Describe the morphology of the erythrocytes.
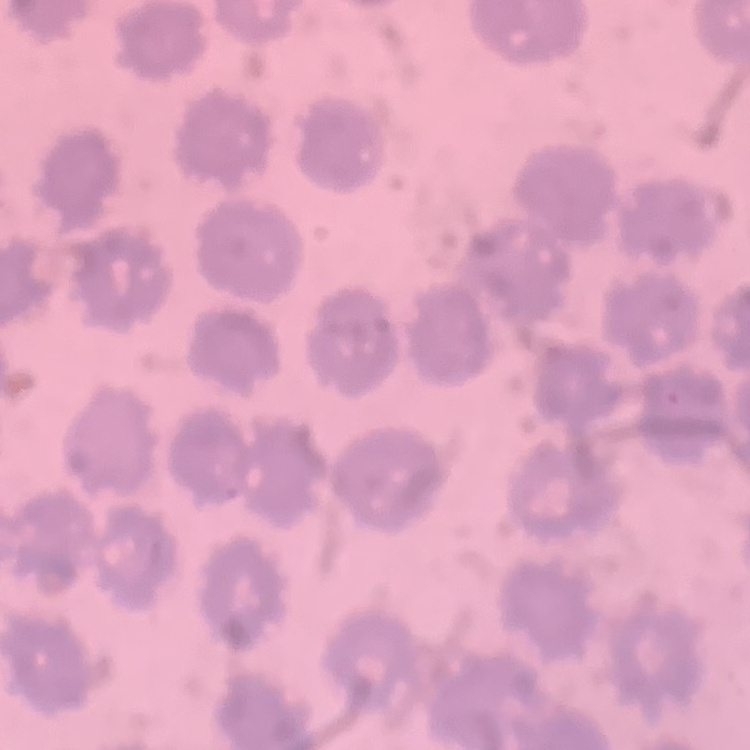
No rouleaux formation.

stain = Field's or Giemsa
preparation = thin peripheral smear
image type = one tile cut from a larger photomicrograph